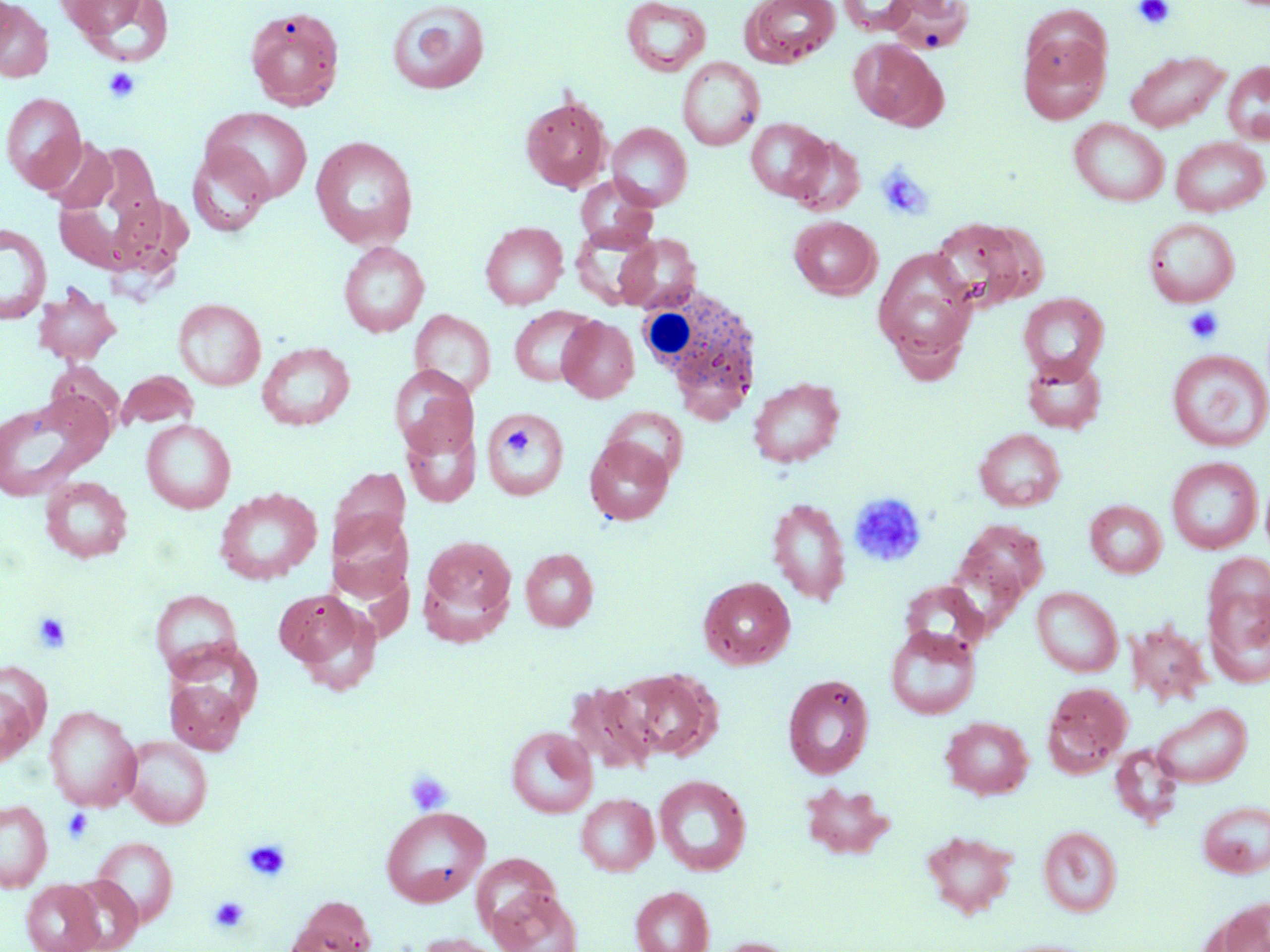
{
  "slide_level_diagnosis": "no evidence of blood parasites",
  "modality": "optical microscopy",
  "field_of_view": "single",
  "uninfected_red_blood_cell_locations": "approximate bounding boxes as named x1/y1/x2/y2 corners in pixels: (x1=60, y1=0, x2=174, y2=66), (x1=621, y1=0, x2=711, y2=76), (x1=741, y1=0, x2=841, y2=67), (x1=838, y1=0, x2=919, y2=35), (x1=888, y1=0, x2=975, y2=54), (x1=386, y1=1, x2=490, y2=95), (x1=0, y1=2, x2=53, y2=81), (x1=244, y1=6, x2=345, y2=111), (x1=1019, y1=32, x2=1110, y2=123), (x1=849, y1=38, x2=947, y2=129), (x1=1124, y1=50, x2=1230, y2=132), (x1=677, y1=56, x2=764, y2=150), (x1=1222, y1=61, x2=1270, y2=144), (x1=1, y1=92, x2=86, y2=192), (x1=520, y1=94, x2=612, y2=193), (x1=202, y1=107, x2=312, y2=203), (x1=1069, y1=118, x2=1170, y2=207), (x1=745, y1=119, x2=831, y2=201), (x1=607, y1=122, x2=692, y2=210), (x1=785, y1=134, x2=865, y2=216), (x1=310, y1=136, x2=418, y2=250), (x1=1170, y1=136, x2=1268, y2=216), (x1=40, y1=137, x2=120, y2=213), (x1=186, y1=146, x2=274, y2=236), (x1=575, y1=175, x2=657, y2=250), (x1=789, y1=216, x2=881, y2=299), (x1=1143, y1=217, x2=1240, y2=307), (x1=929, y1=218, x2=1034, y2=312), (x1=480, y1=221, x2=568, y2=309), (x1=571, y1=223, x2=661, y2=309), (x1=0, y1=224, x2=51, y2=324), (x1=615, y1=233, x2=701, y2=313), (x1=338, y1=241, x2=429, y2=337), (x1=873, y1=247, x2=979, y2=366), (x1=32, y1=286, x2=121, y2=366), (x1=1018, y1=292, x2=1109, y2=381), (x1=173, y1=298, x2=265, y2=390), (x1=510, y1=306, x2=599, y2=387), (x1=409, y1=309, x2=496, y2=398), (x1=558, y1=316, x2=639, y2=403), (x1=257, y1=342, x2=355, y2=430), (x1=1166, y1=349, x2=1269, y2=452), (x1=1022, y1=355, x2=1107, y2=434), (x1=389, y1=365, x2=478, y2=458), (x1=117, y1=370, x2=198, y2=431), (x1=748, y1=377, x2=845, y2=468), (x1=0, y1=395, x2=107, y2=502), (x1=603, y1=406, x2=688, y2=482), (x1=482, y1=408, x2=569, y2=500), (x1=401, y1=416, x2=481, y2=507), (x1=141, y1=419, x2=236, y2=513), (x1=975, y1=428, x2=1066, y2=511), (x1=584, y1=436, x2=674, y2=525), (x1=1167, y1=457, x2=1262, y2=554), (x1=40, y1=476, x2=133, y2=562), (x1=215, y1=487, x2=322, y2=585), (x1=767, y1=497, x2=851, y2=606), (x1=1085, y1=500, x2=1167, y2=578), (x1=327, y1=509, x2=414, y2=601), (x1=953, y1=518, x2=1049, y2=610), (x1=418, y1=535, x2=518, y2=643), (x1=520, y1=548, x2=599, y2=631), (x1=1201, y1=557, x2=1269, y2=689), (x1=699, y1=576, x2=795, y2=669), (x1=901, y1=582, x2=988, y2=659), (x1=1032, y1=586, x2=1123, y2=676), (x1=274, y1=589, x2=376, y2=683), (x1=151, y1=590, x2=242, y2=677), (x1=1127, y1=621, x2=1212, y2=707), (x1=885, y1=625, x2=981, y2=720), (x1=614, y1=668, x2=720, y2=762), (x1=783, y1=674, x2=874, y2=779), (x1=0, y1=675, x2=40, y2=768), (x1=166, y1=678, x2=245, y2=754), (x1=567, y1=681, x2=659, y2=775), (x1=1042, y1=681, x2=1133, y2=776), (x1=1151, y1=702, x2=1252, y2=788), (x1=44, y1=705, x2=141, y2=811), (x1=941, y1=716, x2=1034, y2=799), (x1=506, y1=726, x2=597, y2=818), (x1=122, y1=736, x2=212, y2=829), (x1=1110, y1=742, x2=1183, y2=827), (x1=654, y1=774, x2=751, y2=875), (x1=799, y1=782, x2=895, y2=860), (x1=576, y1=793, x2=658, y2=875), (x1=0, y1=800, x2=53, y2=891), (x1=1198, y1=800, x2=1270, y2=878), (x1=381, y1=806, x2=489, y2=907), (x1=1038, y1=826, x2=1122, y2=917), (x1=921, y1=830, x2=1018, y2=918), (x1=91, y1=836, x2=178, y2=926), (x1=65, y1=876, x2=143, y2=952), (x1=20, y1=880, x2=104, y2=952), (x1=488, y1=886, x2=581, y2=952), (x1=630, y1=886, x2=714, y2=952), (x1=285, y1=896, x2=376, y2=952), (x1=1213, y1=897, x2=1269, y2=952), (x1=414, y1=932, x2=514, y2=952), (x1=709, y1=937, x2=803, y2=952)",
  "stain": "May-Grünwald-Giemsa",
  "magnification": "1000x",
  "white_blood_cell_locations": "approximate bounding boxes as named x1/y1/x2/y2 corners in pixels: (x1=634, y1=283, x2=764, y2=416)",
  "platelet_locations": "approximate bounding boxes as named x1/y1/x2/y2 corners in pixels: (x1=1134, y1=0, x2=1175, y2=29), (x1=103, y1=67, x2=141, y2=104), (x1=876, y1=162, x2=934, y2=222), (x1=1182, y1=306, x2=1225, y2=345), (x1=506, y1=425, x2=537, y2=461), (x1=849, y1=493, x2=926, y2=567), (x1=32, y1=613, x2=71, y2=653), (x1=404, y1=770, x2=452, y2=816), (x1=62, y1=808, x2=94, y2=843), (x1=243, y1=838, x2=291, y2=883), (x1=209, y1=896, x2=250, y2=932)",
  "preparation": "thin blood smear",
  "image_size": "1270×952 pixels"
}